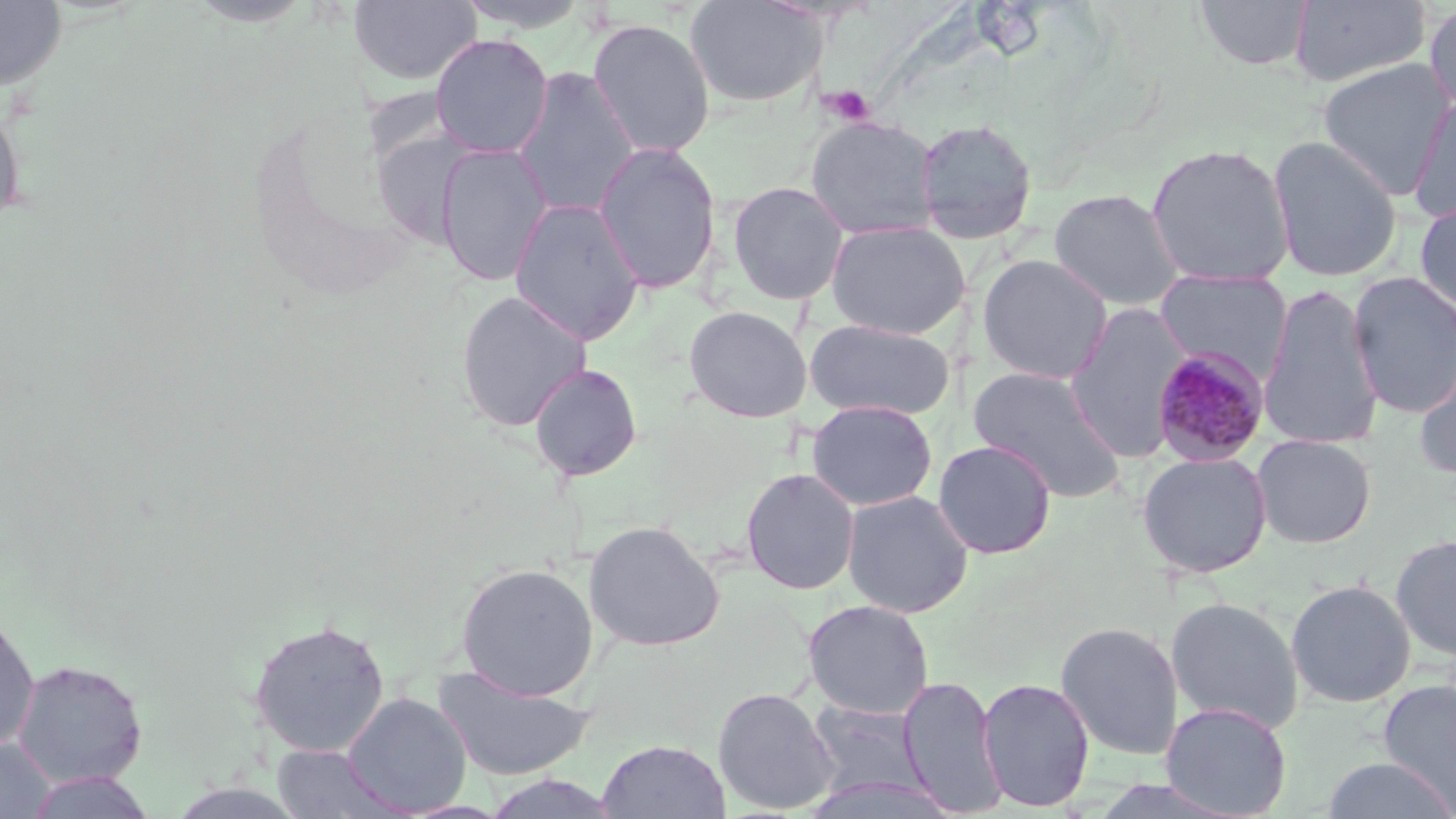

Summary:
  - Coordinate format: approximate bounding boxes as (x1, y1, x2, y2) in pixels
  - Platelet locations: (822, 84, 874, 127)
  - Uninfected red blood cell locations (subset): (0, 0, 67, 93), (348, 0, 483, 87), (453, 0, 596, 33), (684, 0, 823, 108), (1194, 0, 1314, 71), (1288, 0, 1432, 88), (1423, 1, 1456, 116), (587, 17, 715, 158), (429, 34, 553, 158), (1316, 57, 1455, 199), (512, 65, 640, 219), (1408, 94, 1456, 223), (0, 101, 25, 228), (805, 116, 940, 240), (914, 118, 1038, 244), (1267, 135, 1403, 282), (593, 141, 721, 294), (436, 142, 553, 286), (1146, 143, 1295, 288), (728, 181, 849, 305), (1048, 188, 1185, 311), (509, 197, 646, 346), (1414, 198, 1456, 318), (825, 220, 969, 339), (976, 253, 1113, 384), (1154, 268, 1293, 376), (1348, 271, 1456, 419), (1257, 284, 1384, 451), (455, 289, 592, 432), (1064, 302, 1193, 462), (683, 305, 812, 422), (804, 318, 956, 421), (1412, 349, 1456, 481), (528, 363, 643, 481), (968, 365, 1126, 503), (806, 399, 938, 511), (1250, 434, 1377, 549), (933, 439, 1056, 559), (1137, 450, 1273, 578), (740, 467, 859, 594), (842, 489, 974, 617), (583, 520, 724, 651), (1391, 533, 1456, 662), (455, 562, 599, 701), (1285, 579, 1416, 708), (1166, 595, 1305, 735), (802, 599, 934, 719), (0, 613, 40, 755), (247, 619, 391, 757), (1054, 621, 1184, 760), (11, 659, 148, 788), (432, 664, 595, 781), (899, 674, 1006, 816), (977, 677, 1095, 812), (1377, 678, 1456, 814), (712, 686, 840, 815), (342, 692, 472, 816), (805, 699, 931, 801), (1160, 701, 1292, 818), (0, 737, 57, 818), (598, 739, 730, 819), (271, 744, 409, 818), (1319, 756, 1456, 818), (22, 770, 159, 818), (803, 773, 960, 819)
  - Slide-level diagnosis: Plasmodium malariae
  - Modality: light microscopy
  - Preparation: thin blood film
  - Image size: 1456×819 pixels
  - Field of view: single
  - Magnification: 1000x
  - Stain: May-Grünwald-Giemsa